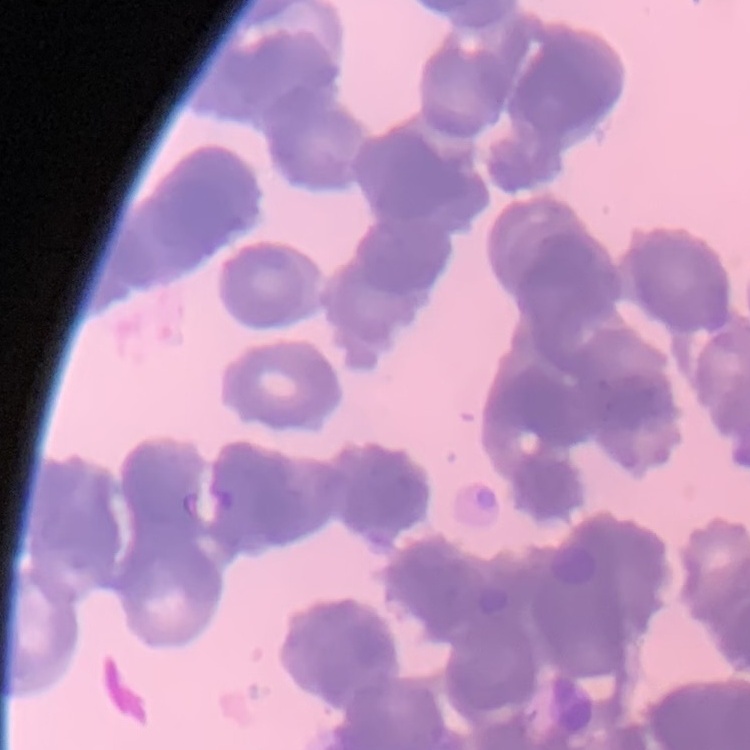
The red blood cells exhibit rouleaux formation. Thin peripheral smear. Square crop of a larger photomicrograph. Stained with either Field's or Giemsa.